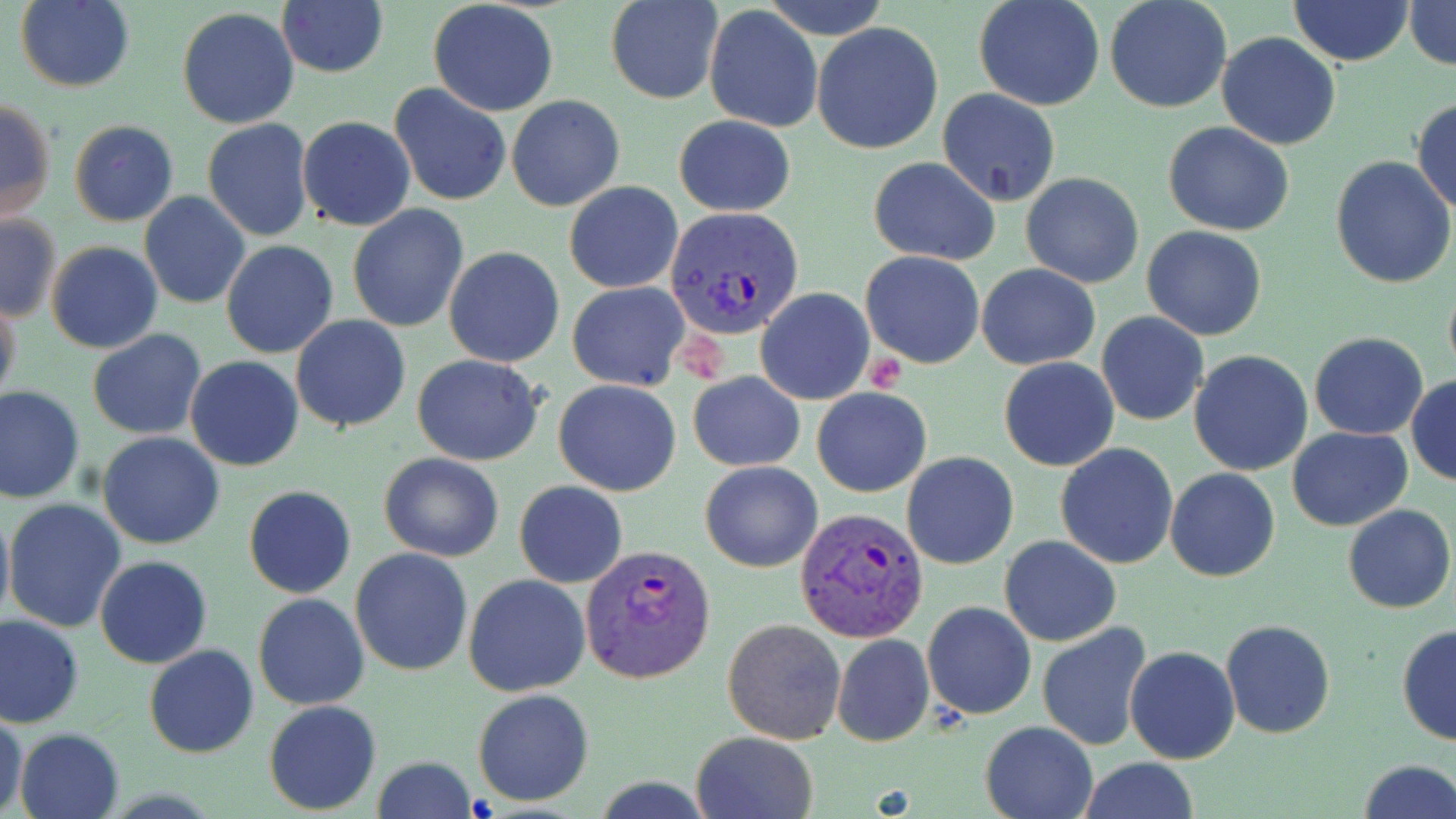
Summary:
  - Coordinate format: approximate bounding boxes as (x1, y1, x2, y2) in pixels
  - Platelet locations: (672, 329, 725, 381), (862, 348, 904, 393)
  - Plasmodium vivax-infected red blood cell locations: (665, 206, 801, 339), (794, 508, 930, 646), (580, 544, 716, 685)
  - Uninfected red blood cell locations: (14, 0, 136, 93), (605, 0, 724, 105), (762, 0, 891, 38), (974, 0, 1106, 110), (1105, 0, 1232, 113), (1288, 0, 1415, 68), (1404, 0, 1455, 70), (427, 1, 559, 117), (276, 2, 389, 79), (704, 4, 822, 132), (177, 7, 301, 130), (813, 22, 943, 155), (1216, 32, 1342, 149), (387, 84, 511, 207), (939, 89, 1060, 205), (507, 95, 625, 211), (0, 97, 56, 225), (1412, 97, 1456, 216), (673, 114, 796, 218), (297, 116, 417, 232), (202, 119, 315, 244), (69, 120, 179, 227), (1163, 122, 1295, 236), (1331, 155, 1456, 289), (867, 158, 1001, 265), (1021, 173, 1145, 289), (563, 180, 684, 294), (140, 191, 250, 309), (347, 203, 469, 333), (0, 214, 61, 322), (1141, 226, 1267, 341), (220, 239, 339, 358), (46, 242, 162, 353), (444, 246, 566, 368), (860, 250, 984, 369), (977, 263, 1100, 371), (1443, 280, 1456, 382), (567, 282, 689, 390), (756, 286, 874, 404), (0, 294, 22, 412), (1096, 312, 1208, 427), (290, 314, 411, 433), (87, 330, 207, 440), (1308, 332, 1430, 439), (1188, 350, 1314, 476), (412, 354, 546, 466), (186, 356, 305, 472), (999, 357, 1119, 471), (688, 371, 805, 472), (1406, 376, 1456, 487), (553, 379, 682, 496), (0, 384, 85, 503), (811, 386, 931, 497), (1287, 426, 1414, 531), (98, 432, 224, 548), (1055, 443, 1179, 569), (903, 451, 1018, 570), (379, 452, 504, 562), (699, 460, 823, 573), (1166, 467, 1281, 582), (514, 481, 627, 588), (243, 486, 357, 598), (4, 499, 125, 632), (0, 503, 13, 632), (1343, 503, 1455, 614), (999, 535, 1122, 647), (349, 548, 473, 677), (95, 555, 212, 668), (464, 573, 591, 696), (253, 593, 371, 710), (922, 600, 1036, 721), (1, 615, 84, 727), (722, 619, 847, 745), (1221, 619, 1335, 739), (1037, 621, 1153, 751), (1396, 626, 1456, 745), (832, 633, 935, 747), (143, 643, 259, 758), (1126, 646, 1239, 765), (472, 689, 594, 805), (263, 700, 381, 815), (0, 708, 27, 818), (979, 720, 1097, 819), (15, 727, 124, 819), (690, 731, 817, 819), (370, 755, 478, 819), (1077, 757, 1200, 818), (1355, 758, 1455, 819)
  - Slide-level diagnosis: Plasmodium vivax
  - Image size: 1456×819 pixels
  - Magnification: 1000x
  - Modality: optical microscopy
  - Field of view: one of a larger specimen
  - Stain: May-Grünwald-Giemsa
  - Preparation: thin blood film